Report the malaria status of this cell.
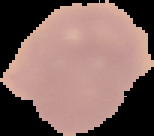

Uninfected.

image_size: 154×136 pixels
image_type: cell region segmented out of the field of view; surrounding area masked to black
preparation: thin blood film